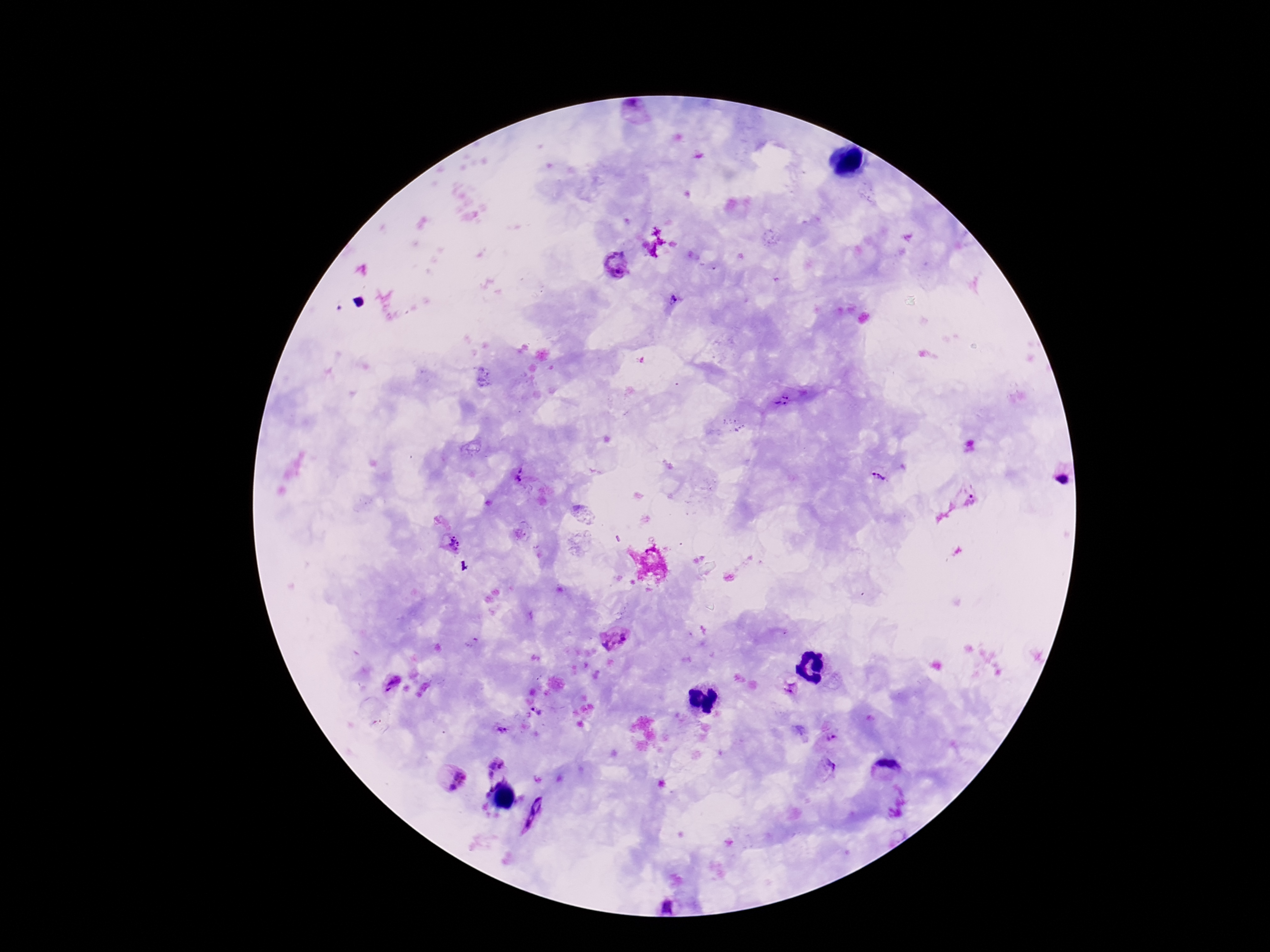

field_of_view: single
image_size: 1270×952 pixels
plasmodium_parasite_locations: 'approximate centers as (x, y) in pixels: (635, 112), (615, 264), (673, 300), (782, 399), (519, 475), (1058, 475), (879, 478), (967, 497), (450, 544), (613, 638), (391, 685), (790, 687), (538, 711), (375, 722), (502, 728), (833, 737), (495, 768), (827, 769), (886, 770), (455, 778), (489, 787), (536, 814), (669, 906)'
stain: Giemsa
magnification: 100x
capture: smartphone camera through the microscope eyepiece
patient_malaria_status: positive
preparation: thick blood smear